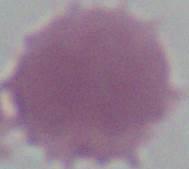 Captured at 1000x magnification. An erythrocyte is shown. Photomicrograph.